Locate every blood parasite and identify its species.
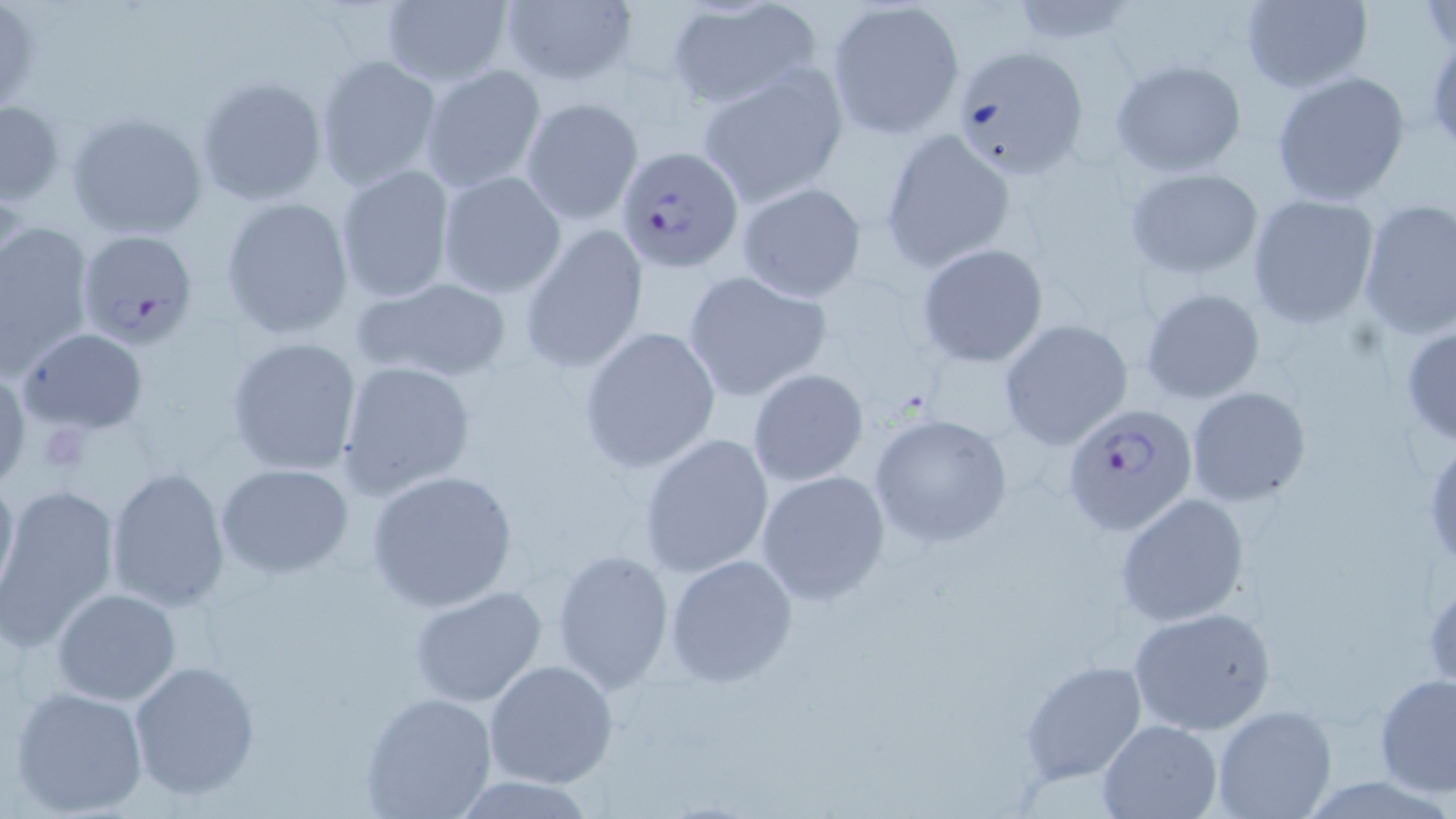

Approximate bounding boxes as (x1, y1, x2, y2) in pixels.
Plasmodium falciparum-infected red blood cells: (615, 145, 744, 273), (77, 230, 200, 348), (1062, 402, 1198, 538).
No Plasmodium ovale, Plasmodium malariae, Plasmodium vivax, Babesia divergens, or Trypanosoma brucei observed.

slide_level_diagnosis: Plasmodium falciparum
preparation: thin blood film
uninfected_red_blood_cell_locations: 'approximate bounding boxes as (x1, y1, x2, y2) in pixels: (499, 0, 638, 89), (1239, 0, 1373, 94), (379, 1, 513, 87), (826, 1, 964, 138), (1423, 1, 1454, 56), (0, 4, 46, 115), (662, 5, 822, 112), (946, 44, 1090, 179), (314, 55, 443, 192), (1108, 58, 1248, 177), (418, 62, 547, 194), (697, 65, 848, 207), (1270, 70, 1411, 207), (195, 75, 328, 207), (520, 97, 643, 225), (0, 100, 64, 205), (65, 112, 207, 241), (880, 128, 1017, 273), (335, 165, 455, 303), (1122, 167, 1264, 279), (436, 170, 567, 299), (735, 181, 867, 302), (1246, 194, 1380, 328), (220, 197, 355, 339), (1357, 199, 1456, 341), (0, 221, 92, 379), (518, 225, 649, 375), (917, 243, 1049, 368), (682, 269, 833, 402), (350, 274, 514, 386), (1139, 287, 1266, 404), (998, 319, 1133, 450), (1400, 324, 1456, 449), (577, 326, 721, 473), (17, 327, 149, 434), (225, 336, 363, 476), (336, 361, 479, 501), (0, 364, 30, 492), (747, 368, 870, 486), (1185, 386, 1312, 508), (869, 413, 1013, 546), (638, 432, 775, 582), (1424, 440, 1456, 573), (215, 464, 353, 578), (1, 466, 19, 609), (104, 466, 231, 611), (366, 470, 519, 612), (756, 470, 890, 605), (1, 486, 121, 650), (1116, 493, 1252, 628), (551, 547, 674, 692), (665, 553, 798, 688), (409, 585, 550, 711), (51, 588, 182, 707), (1127, 605, 1280, 738), (483, 659, 619, 789), (1017, 659, 1146, 786), (127, 660, 260, 801), (1374, 671, 1455, 797), (9, 684, 150, 816), (358, 691, 497, 818), (1211, 705, 1338, 819), (1096, 719, 1222, 819), (451, 775, 596, 817)'
stain: May-Grünwald-Giemsa
modality: light microscopy
image_size: 1456×819 pixels
magnification: 1000x
platelet_locations: 'approximate bounding boxes as (x1, y1, x2, y2) in pixels: (39, 419, 94, 475)'
field_of_view: one of a larger specimen